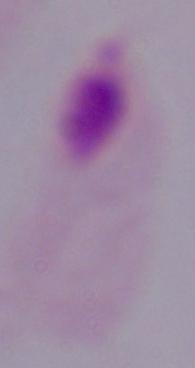

modality = micrograph
magnification = 1000x
identification = trichomonad